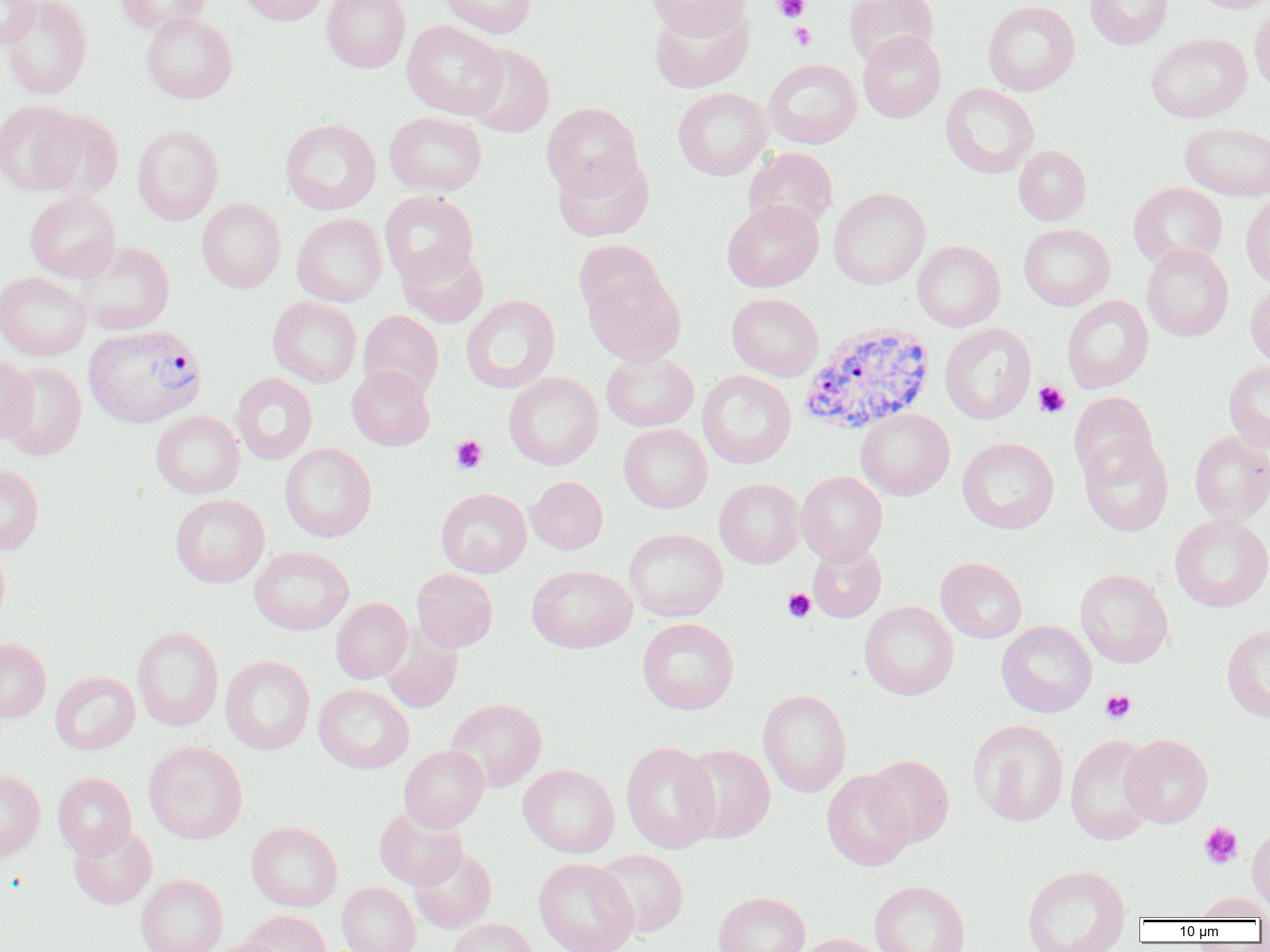

Approximate bounding boxes as (x1, y1, x2, y2) in pixels. Platelet locations: (772, 0, 811, 23), (789, 23, 816, 50), (1033, 381, 1070, 418), (450, 435, 487, 473), (782, 588, 816, 623), (1100, 690, 1136, 723), (1199, 822, 1243, 869). Plasmodium vivax-infected red blood cell locations: (799, 320, 936, 435), (83, 323, 206, 428). Uninfected red blood cell locations: (0, 0, 40, 51), (1, 0, 92, 99), (116, 0, 212, 35), (235, 0, 331, 26), (322, 0, 411, 73), (441, 0, 537, 38), (645, 0, 753, 38), (843, 0, 938, 66), (983, 0, 1080, 96), (1084, 0, 1173, 49), (1191, 0, 1270, 13), (649, 2, 754, 93), (1249, 2, 1270, 95), (141, 12, 237, 103), (402, 20, 507, 119), (858, 30, 946, 122), (1146, 32, 1251, 123), (464, 43, 555, 137), (763, 58, 862, 148), (940, 83, 1039, 178), (673, 87, 771, 180), (0, 101, 87, 195), (542, 102, 644, 199), (34, 109, 126, 200), (385, 111, 487, 195), (280, 118, 381, 214), (1179, 121, 1270, 200), (132, 125, 224, 225), (1013, 145, 1091, 225), (743, 147, 839, 232), (552, 152, 654, 242), (1128, 182, 1228, 269), (828, 187, 930, 289), (380, 190, 479, 285), (25, 192, 121, 282), (1241, 192, 1270, 287), (196, 197, 286, 293), (722, 199, 823, 292), (292, 213, 388, 306), (1018, 223, 1115, 310), (573, 239, 664, 322), (913, 240, 1005, 331), (75, 242, 175, 335), (397, 243, 489, 327), (1141, 244, 1233, 341), (584, 269, 685, 365), (0, 271, 91, 360), (1245, 281, 1270, 367), (727, 293, 824, 381), (461, 294, 560, 393), (1062, 295, 1153, 393), (267, 296, 362, 387), (358, 310, 444, 399), (940, 323, 1036, 424), (601, 352, 699, 431), (0, 355, 38, 444), (1223, 360, 1270, 451), (2, 361, 88, 461), (346, 365, 435, 450), (696, 370, 796, 469), (503, 372, 604, 469), (231, 373, 317, 464), (1068, 392, 1157, 481), (855, 408, 955, 500), (151, 410, 245, 498), (618, 424, 712, 513), (1189, 431, 1270, 524), (1078, 435, 1173, 536), (957, 437, 1059, 534), (280, 442, 376, 541), (0, 464, 44, 553), (796, 471, 887, 565), (526, 476, 608, 554), (714, 478, 805, 568), (436, 488, 531, 577), (170, 494, 269, 587), (1169, 513, 1270, 612), (624, 528, 728, 621), (808, 542, 887, 622), (0, 545, 10, 632), (249, 545, 354, 635), (935, 557, 1027, 643), (527, 564, 637, 653), (411, 568, 498, 652), (1075, 568, 1173, 668), (331, 598, 412, 684), (859, 601, 958, 700), (637, 618, 739, 714), (996, 620, 1097, 717), (1221, 623, 1270, 722), (132, 626, 223, 731), (380, 626, 462, 713), (0, 639, 51, 723), (220, 655, 315, 754), (50, 671, 139, 755), (313, 684, 414, 773), (758, 689, 852, 797), (446, 698, 547, 791), (968, 719, 1068, 827), (1120, 733, 1213, 828), (1064, 735, 1159, 845), (144, 741, 247, 844), (621, 741, 721, 853), (679, 744, 776, 843), (399, 745, 489, 832), (864, 755, 954, 848), (518, 764, 619, 858), (0, 769, 45, 860), (822, 769, 915, 871), (52, 772, 136, 858), (374, 806, 468, 889), (68, 821, 156, 909), (246, 822, 343, 910), (1247, 825, 1270, 913), (409, 845, 497, 933), (594, 849, 688, 938), (534, 857, 638, 952), (1022, 865, 1131, 952), (135, 874, 227, 952), (869, 880, 970, 952), (336, 882, 421, 952), (713, 891, 810, 952), (1194, 893, 1270, 920), (243, 910, 331, 952), (448, 918, 537, 952), (791, 933, 886, 952), (205, 938, 287, 952). Slide-level diagnosis: Plasmodium vivax. Light microscopy. Single field of view. Thin blood film. Image is 1270×952 pixels. 1000x magnification.